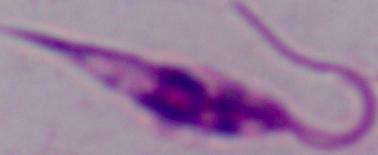

Captured at 1000x magnification. A Leishmania parasite is seen. Micrograph.